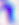

Summary:
  - Modality: photomicrograph
  - Identification: Toxoplasma gondii
  - Magnification: 400x